Comment on the morphology of the red blood cells.
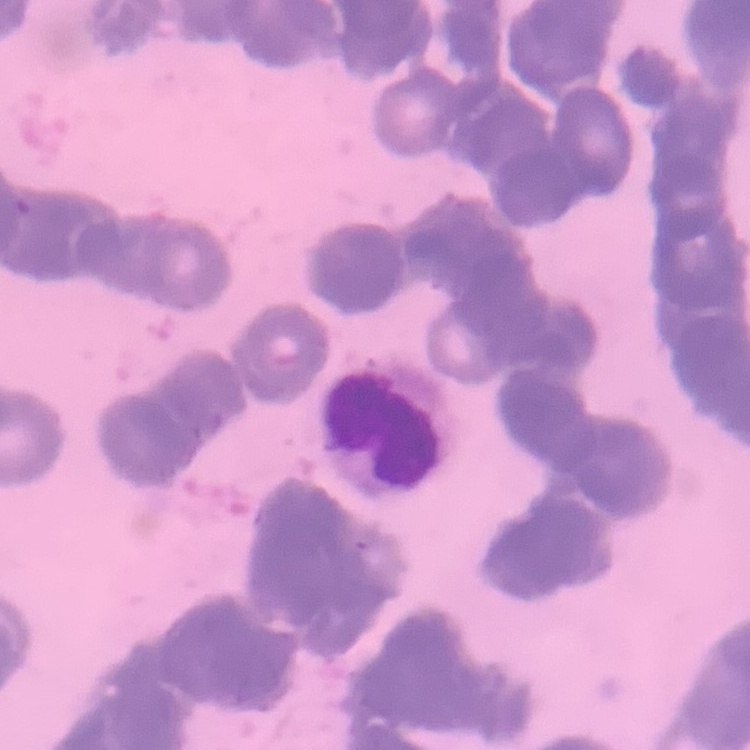

They show rouleaux formation.

{
  "stain": "Field's or Giemsa",
  "preparation": "thin blood smear",
  "image_type": "square crop of a larger photomicrograph"
}